Classify this cell by malaria status.
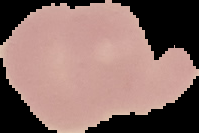

Uninfected.

From a thin blood smear. Image is 199×133 pixels. Segmented cell region on a black background.